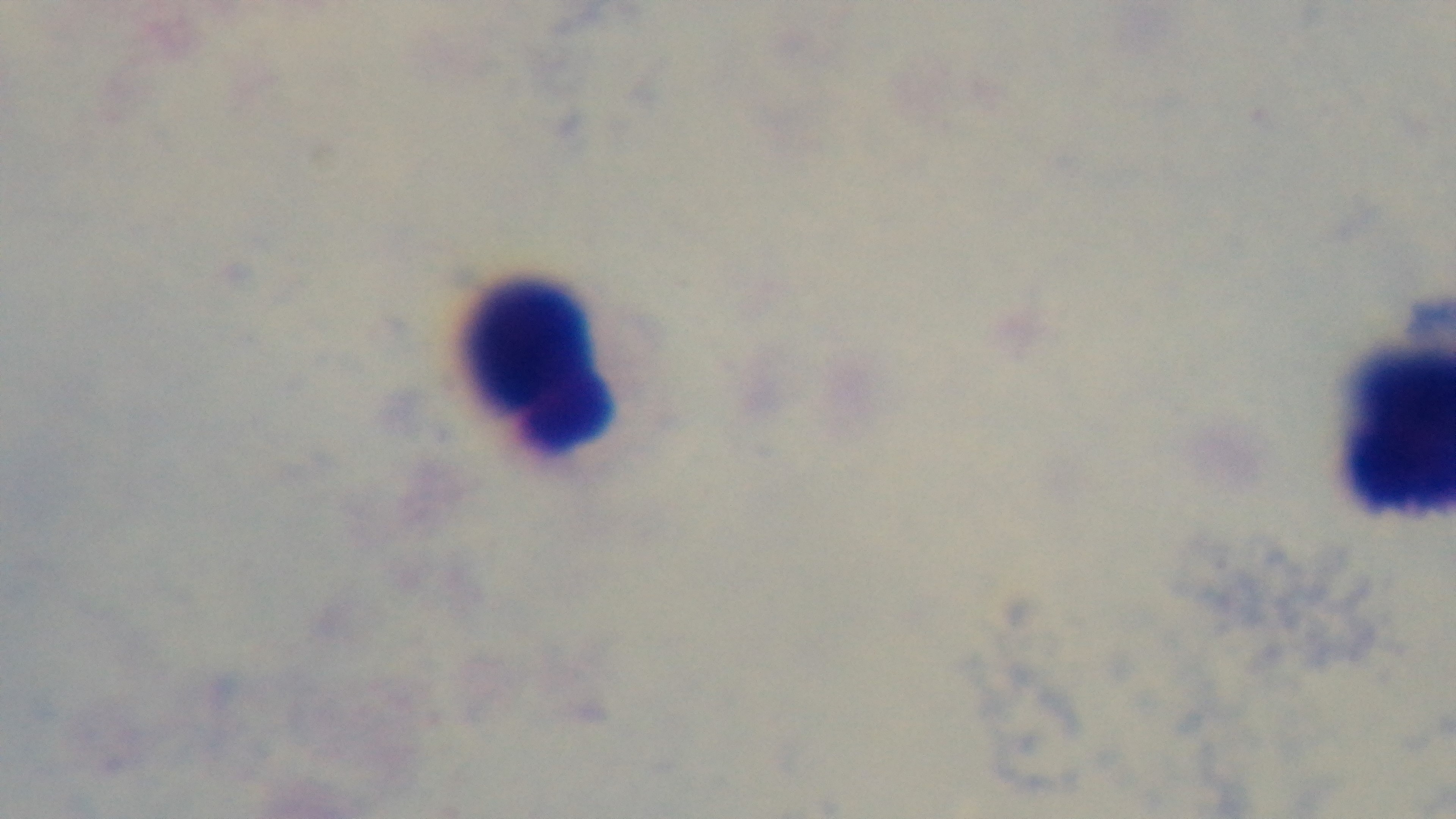

Summary:
  - Field of view: single
  - Modality: light microscopy
  - Malaria status: negative
  - Objective: 100x oil immersion
  - Preparation: thick
  - Stain: Giemsa
  - Capture: mounted 4K digital camera